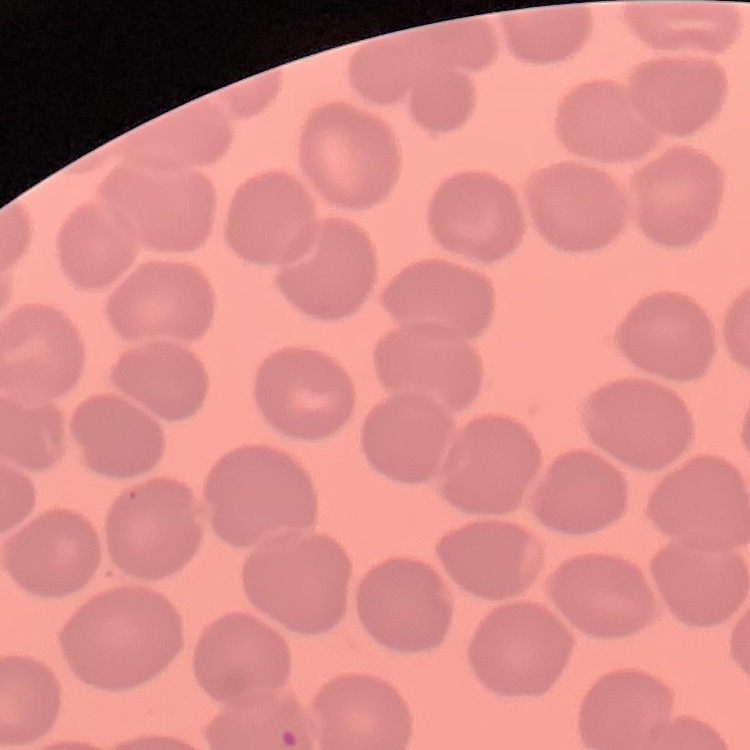
red blood cell morphology = no rouleaux formation
image type = one tile cut from a larger photomicrograph
stain = Field's or Giemsa
preparation = thin peripheral smear